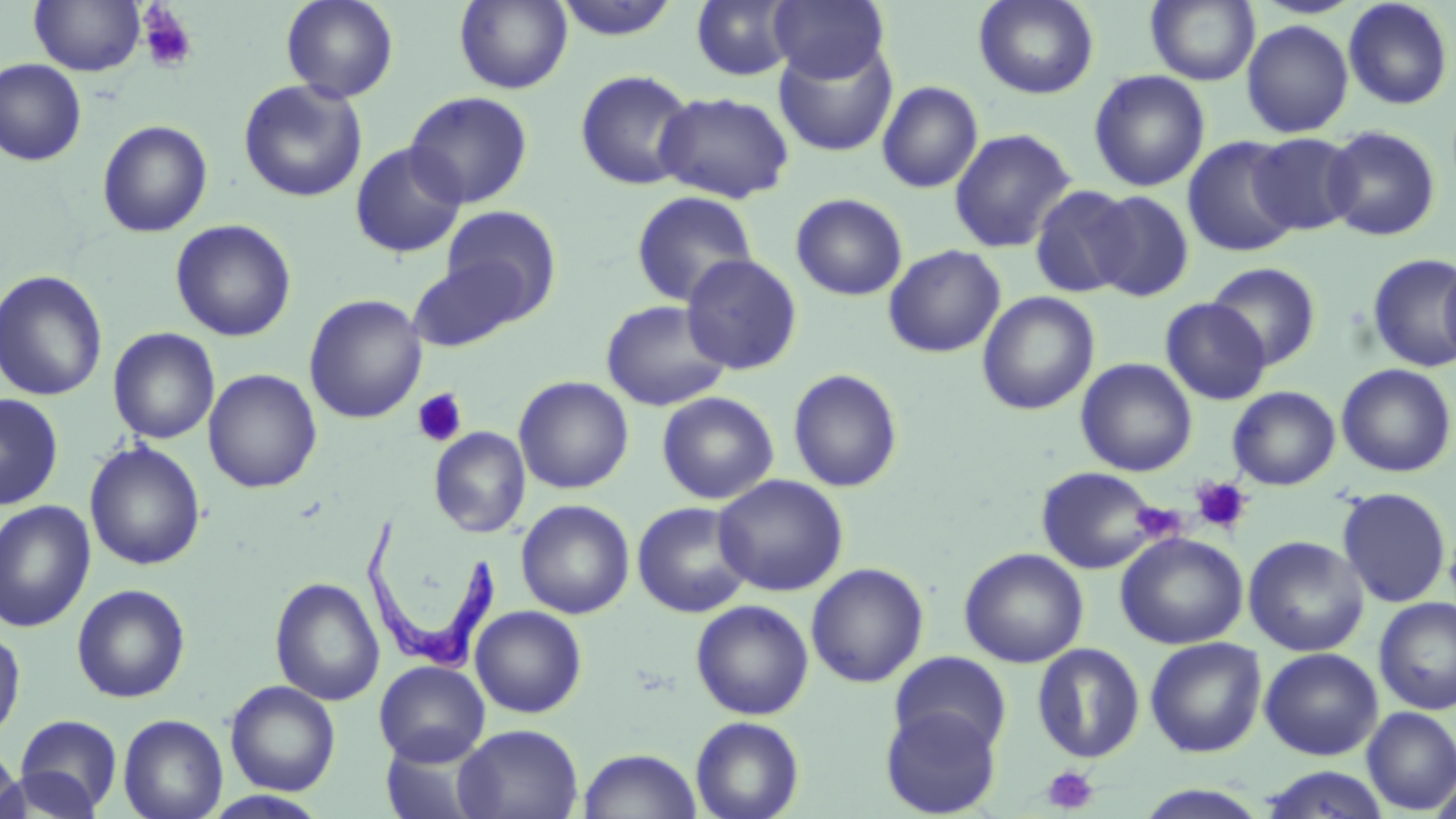
slide-level diagnosis = Trypanosoma brucei
magnification = 1000x
uninfected red blood cell locations = approximate bounding boxes as (x1,y1)-(x2,y2) corner pairs in pixels: (30,0)-(145,76), (281,0)-(399,103), (454,0)-(573,93), (552,0)-(683,41), (769,0)-(889,84), (973,0)-(1098,99), (1146,0)-(1260,85), (1342,0)-(1454,110), (691,1)-(797,80), (1241,19)-(1354,138), (774,41)-(898,157), (0,58)-(87,166), (575,69)-(698,191), (1088,70)-(1210,192), (237,79)-(368,203), (877,81)-(984,193), (654,90)-(795,204), (404,91)-(534,208), (97,119)-(213,237), (1322,125)-(1441,241), (949,128)-(1077,253), (1249,132)-(1360,235), (1182,136)-(1301,258), (349,141)-(466,259), (1029,184)-(1139,298), (630,190)-(759,307), (1086,190)-(1194,302), (790,193)-(908,301), (440,205)-(562,319), (170,219)-(296,341), (884,244)-(1006,358), (1366,253)-(1456,372), (1439,253)-(1456,372), (681,254)-(803,375), (408,259)-(527,351), (1206,262)-(1321,369), (0,270)-(108,401), (977,291)-(1100,415), (303,294)-(428,423), (1161,298)-(1271,404), (600,299)-(731,411), (107,327)-(220,444), (1076,358)-(1197,477), (1336,364)-(1456,477), (203,368)-(322,493), (787,368)-(903,492), (513,376)-(634,494), (1227,386)-(1341,490), (657,391)-(779,504), (0,393)-(63,510), (429,427)-(530,538), (84,441)-(206,570), (1036,466)-(1162,574), (713,474)-(849,596), (1336,487)-(1452,608), (516,499)-(635,619), (0,500)-(96,632), (632,501)-(755,618), (1115,532)-(1248,649), (1243,536)-(1369,656), (959,547)-(1088,668), (806,562)-(929,688), (270,577)-(385,706), (72,583)-(191,703), (1374,597)-(1456,715), (690,599)-(814,720), (470,605)-(587,718), (0,624)-(26,744), (1145,637)-(1267,758), (1032,643)-(1145,763), (1259,647)-(1384,760), (889,651)-(1013,756), (374,661)-(490,766), (225,680)-(340,796), (880,706)-(1002,818), (1361,707)-(1456,814), (13,714)-(124,815), (118,714)-(228,819), (690,716)-(805,819), (454,724)-(583,819), (0,741)-(25,819), (578,748)-(702,819), (1257,766)-(1391,818), (2,767)-(103,818), (1132,785)-(1272,818), (202,791)-(331,819)
stain = May-Grünwald-Giemsa
modality = light microscopy
preparation = thin blood smear
field of view = one of a larger specimen
platelet locations = approximate bounding boxes as (x1,y1)-(x2,y2) corner pairs in pixels: (137,5)-(199,75), (411,387)-(468,448), (1190,476)-(1254,536), (1133,499)-(1185,543), (1042,765)-(1100,814)
image size = 1456×819 pixels
Trypanosoma brucei locations = approximate bounding boxes as (x1,y1)-(x2,y2) corner pairs in pixels: (360,514)-(501,677)